Assess the morphology of the red blood cells.
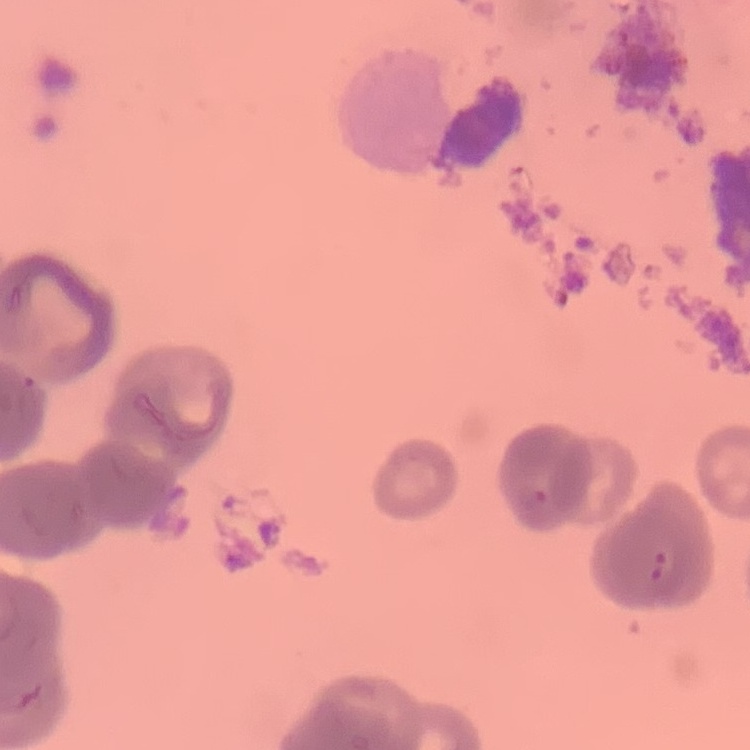

They show rouleaux formation.

preparation = thin blood film
stain = Field's or Giemsa
image type = one tile cut from a larger photomicrograph